Report the malaria status of this cell.
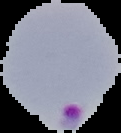
It is parasitized.

Summary:
  - Preparation: thin blood smear
  - Image size: 121×133 pixels
  - Image type: cell region segmented out of the field of view; surrounding area masked to black